State the blood parasite species.
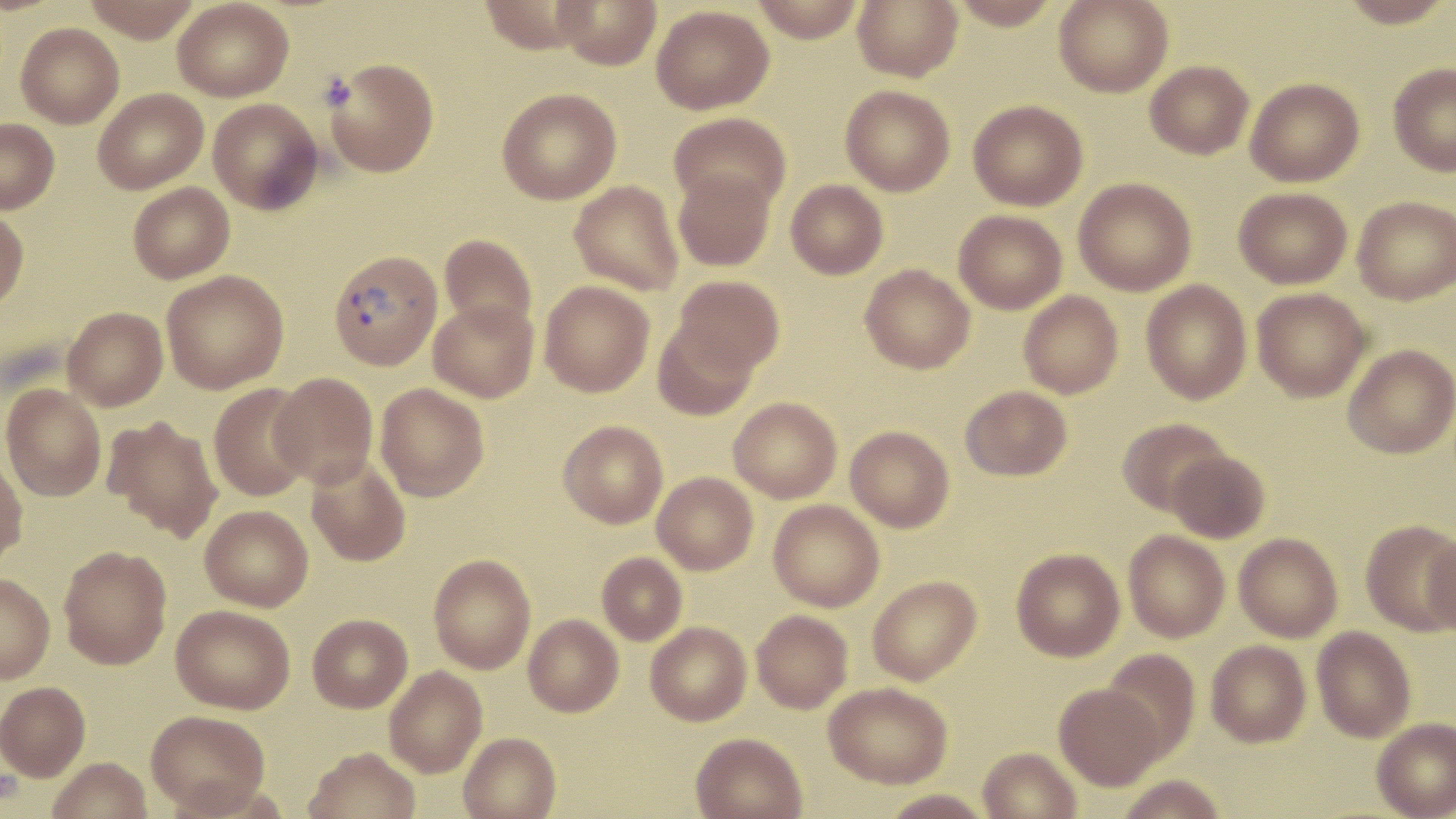

Plasmodium vivax.

field_of_view: one of a larger specimen
plasmodium_vivax_infected_red_blood_cell_locations: 'approximate bounding boxes as [x1, y1, x2, y2] in pixels: [328, 248, 442, 370]'
preparation: thin blood film
image_size: 1456×819 pixels
platelet_locations: 'approximate bounding boxes as [x1, y1, x2, y2] in pixels: [316, 72, 355, 111]'
stain: May-Grünwald-Giemsa
magnification: 1000x
uninfected_red_blood_cell_locations: 'approximate bounding boxes as [x1, y1, x2, y2] in pixels: [81, 0, 204, 43], [477, 0, 600, 54], [553, 0, 662, 70], [749, 0, 866, 42], [852, 0, 962, 82], [947, 0, 1062, 30], [1054, 0, 1173, 98], [1339, 0, 1453, 28], [172, 1, 293, 102], [651, 5, 774, 115], [15, 22, 124, 128], [324, 58, 439, 178], [1145, 60, 1254, 159], [1388, 62, 1456, 176], [1245, 77, 1364, 187], [840, 85, 956, 196], [93, 88, 208, 194], [496, 88, 622, 205], [208, 98, 323, 214], [968, 99, 1088, 211], [670, 113, 791, 213], [0, 118, 59, 214], [673, 169, 775, 272], [1073, 177, 1197, 296], [786, 180, 888, 280], [569, 181, 684, 296], [128, 183, 234, 284], [1233, 186, 1352, 289], [1352, 196, 1455, 305], [0, 208, 29, 313], [953, 210, 1068, 314], [439, 234, 537, 335], [860, 263, 975, 374], [161, 270, 289, 393], [672, 275, 785, 376], [1141, 280, 1253, 405], [539, 281, 654, 397], [1251, 288, 1370, 402], [1018, 290, 1123, 399], [428, 299, 539, 403], [62, 307, 168, 411], [653, 320, 760, 420], [1343, 344, 1455, 459], [270, 372, 378, 488], [1, 383, 106, 502], [208, 383, 313, 502], [375, 383, 489, 501], [960, 385, 1073, 481], [729, 397, 842, 503], [103, 415, 224, 542], [1117, 417, 1231, 517], [558, 420, 668, 528], [846, 426, 955, 532], [1166, 449, 1271, 543], [0, 453, 28, 571], [306, 456, 411, 567], [652, 472, 758, 575], [768, 499, 885, 612], [200, 505, 313, 612], [1360, 520, 1456, 637], [1422, 529, 1456, 639], [1123, 530, 1231, 642], [1234, 532, 1343, 642], [58, 545, 172, 669], [1011, 548, 1125, 662], [597, 553, 687, 646], [428, 554, 536, 674], [0, 573, 55, 684], [867, 575, 981, 685], [171, 604, 295, 714], [751, 609, 853, 713], [307, 614, 412, 713], [523, 614, 623, 717], [645, 622, 752, 726], [1312, 626, 1416, 742], [1206, 639, 1312, 748], [1101, 649, 1201, 762], [384, 666, 487, 778], [0, 681, 90, 781], [823, 682, 952, 789], [1054, 683, 1165, 790], [146, 710, 270, 814], [1372, 718, 1456, 819], [458, 731, 561, 819], [691, 732, 808, 819], [303, 746, 422, 819], [978, 747, 1082, 819], [47, 757, 152, 819], [1113, 774, 1230, 819], [878, 789, 994, 818]'
modality: light microscopy